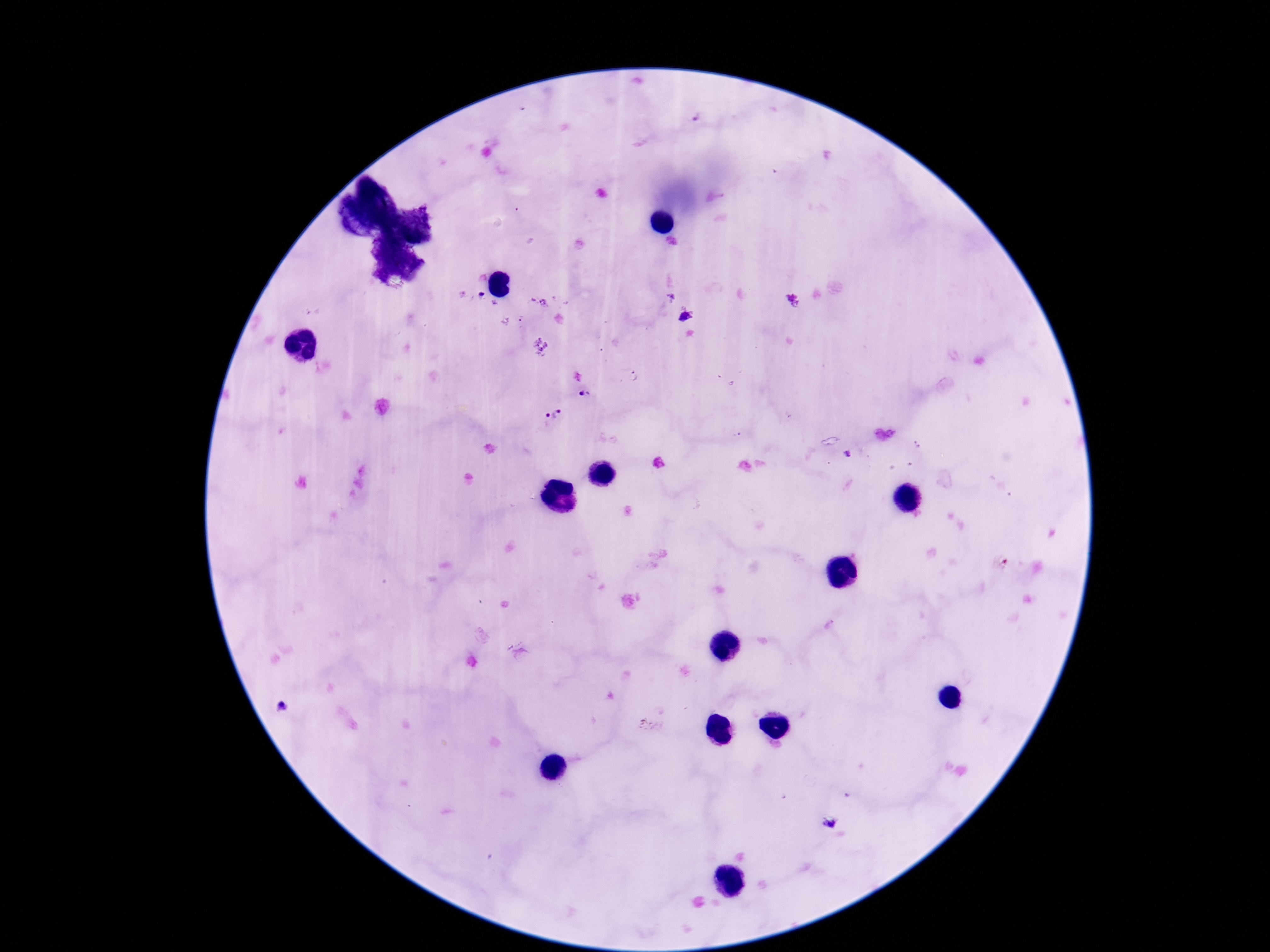
Approximate centers as {x, y} in pixels.
Summary:
  - Plasmodium parasite locations: {685, 316}, {586, 392}, {554, 415}, {829, 822}
  - Magnification: 100x
  - Patient malaria status: positive
  - Preparation: thick peripheral-blood smear
  - Capture: smartphone camera through the microscope eyepiece
  - Stain: Giemsa
  - Image size: 1270×952 pixels
  - Field of view: one from this slide